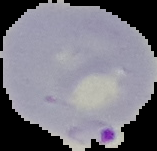 Malaria status: parasitized. Image is 157×151 pixels. From a thin blood film. Cell region segmented out of the field of view; the surrounding area is masked to black.